Locate every Plasmodium parasite by life-cycle stage, and every leukocyte.
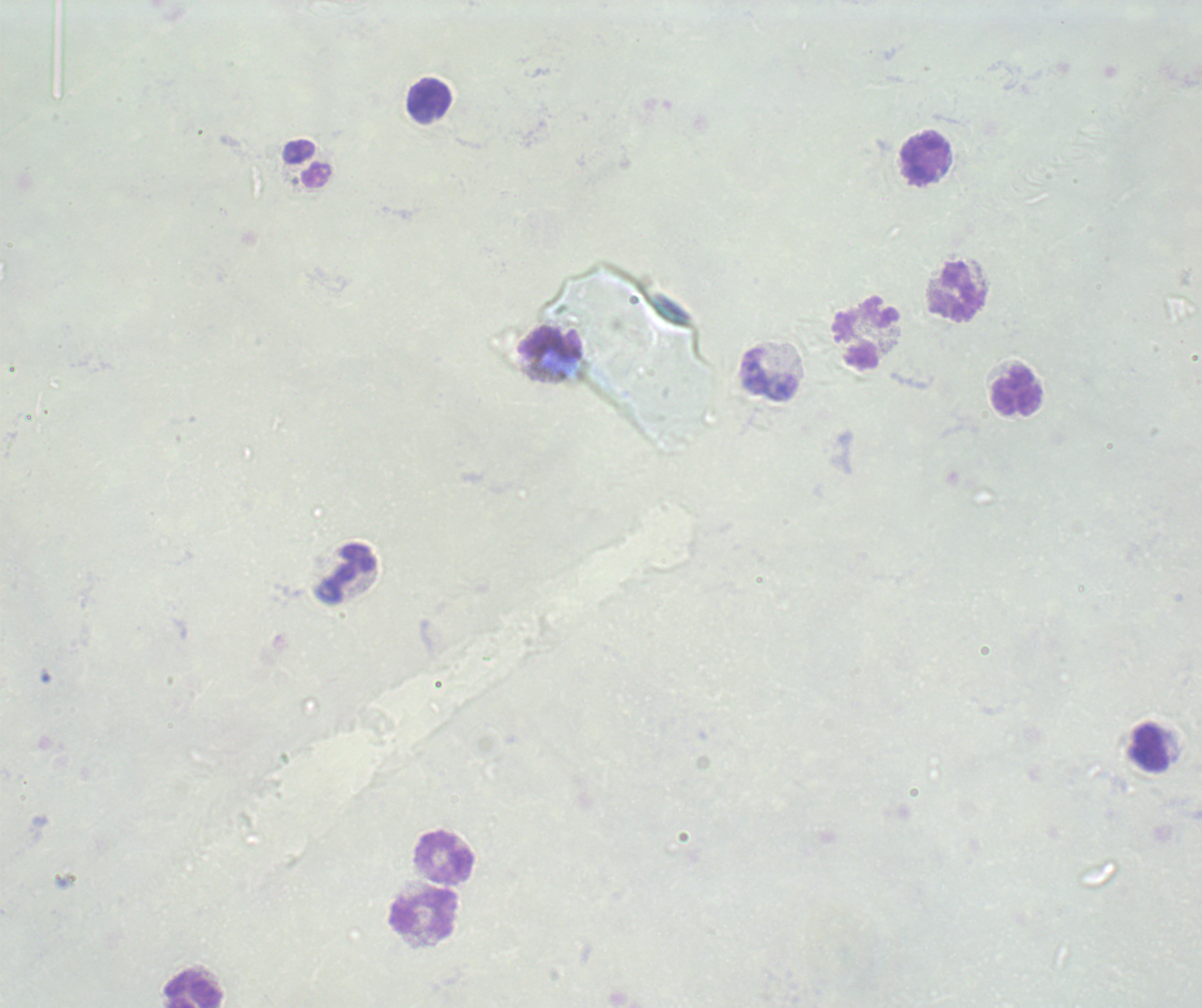

No Plasmodium parasites detected.
Approximate object centers, in pixels from the top-left corner.
Leukocytes: (x=430, y=97), (x=922, y=159), (x=307, y=164), (x=955, y=290), (x=867, y=336), (x=551, y=345), (x=769, y=376), (x=1017, y=392), (x=347, y=573), (x=1148, y=748), (x=444, y=856), (x=424, y=913), (x=194, y=989).

Background quality: poor. Single field of view. Previously used in an actual diagnosis. Captured at 100x magnification. Image is 1202×1008 pixels. Romanowsky-stained preparation. Thick blood smear.